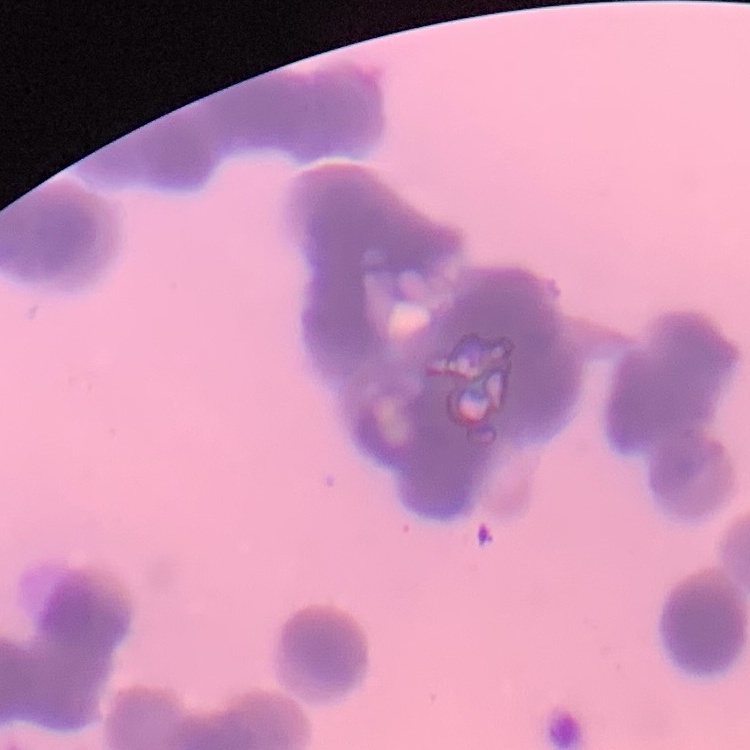 The red blood cells show rouleaux formation. Field's or Giemsa stain. Thin peripheral smear. One tile cut from a larger photomicrograph.